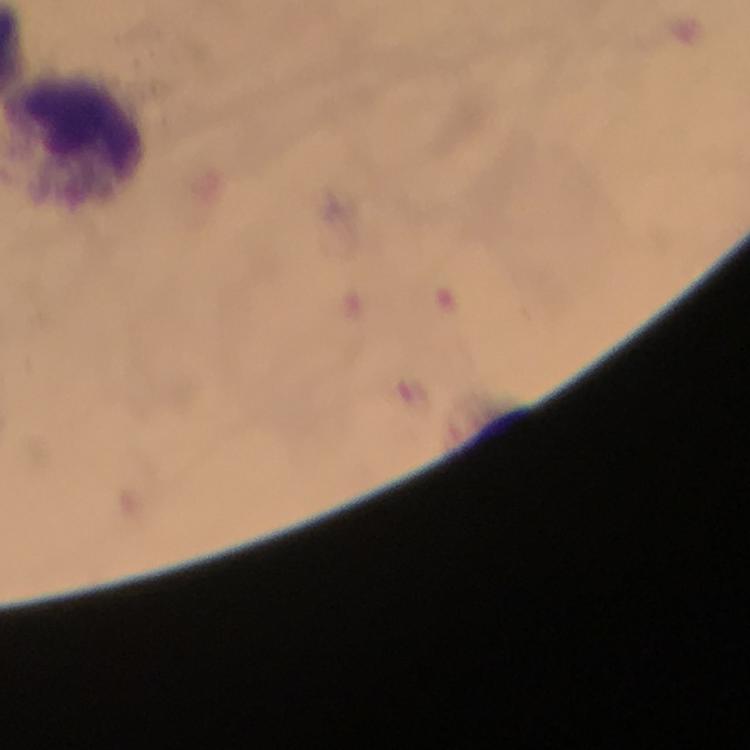
Approximate centers as [x, y] in pixels.
Summary:
  - Leukocyte locations: [75, 135]
  - Image size: 750×750 pixels
  - Malaria parasites: none seen
  - Immersion oil: used
  - Preparation: thick blood smear
  - Capture: smartphone camera through the microscope
  - Magnification: 100x
  - Cropped from: a single field of view
  - Stain: Giemsa
  - Context: from a malaria diagnostic workup